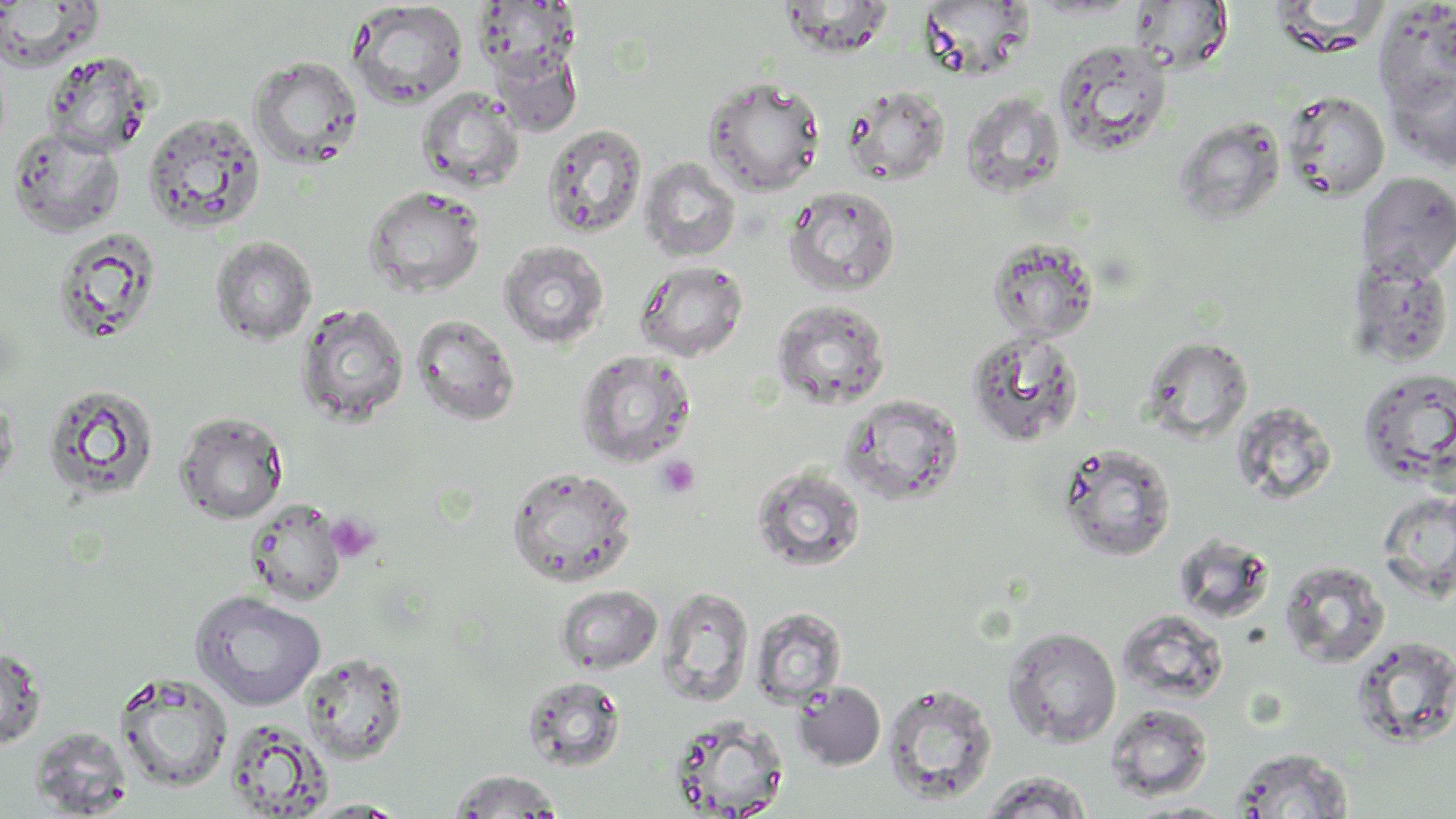

Summary:
  - Coordinate format: approximate bounding boxes as [x1, y1, x2, y2] in pixels
  - Platelet locations: [656, 455, 700, 498], [326, 513, 380, 563]
  - Uninfected red blood cell locations: [779, 0, 896, 58], [0, 1, 104, 72], [346, 1, 469, 109], [919, 1, 1035, 81], [1130, 1, 1233, 74], [475, 2, 581, 84], [1373, 2, 1456, 111], [1053, 39, 1174, 157], [493, 47, 582, 137], [43, 51, 153, 157], [248, 56, 364, 170], [1386, 67, 1456, 172], [703, 77, 825, 197], [842, 84, 951, 186], [416, 86, 524, 193], [1281, 89, 1390, 201], [959, 91, 1066, 200], [143, 112, 267, 236], [1173, 116, 1286, 226], [542, 124, 648, 239], [7, 127, 126, 238], [639, 158, 742, 262], [1356, 172, 1456, 284], [363, 185, 487, 298], [784, 185, 901, 296], [51, 228, 164, 347], [210, 236, 317, 346], [986, 237, 1099, 343], [497, 240, 610, 350], [1347, 256, 1455, 369], [634, 260, 749, 362], [771, 298, 890, 409], [295, 301, 410, 428], [411, 313, 521, 426], [965, 329, 1084, 447], [1143, 336, 1254, 441], [574, 348, 697, 468], [1356, 368, 1456, 488], [41, 383, 161, 503], [0, 390, 20, 499], [839, 394, 964, 506], [174, 411, 289, 524], [1057, 443, 1177, 562], [750, 463, 867, 573], [506, 465, 637, 587], [1376, 490, 1455, 600], [245, 498, 347, 606], [1279, 559, 1390, 668], [554, 584, 663, 674], [658, 586, 755, 707], [189, 590, 327, 710], [750, 606, 847, 708], [1118, 609, 1230, 706], [1004, 626, 1121, 747], [1349, 635, 1456, 748], [0, 646, 47, 751], [301, 651, 409, 764], [114, 672, 234, 793], [521, 674, 627, 773], [793, 682, 886, 770], [881, 682, 998, 805], [1105, 704, 1213, 801], [666, 713, 789, 818], [224, 718, 333, 817], [30, 727, 133, 817], [1230, 747, 1355, 818], [446, 769, 565, 817], [980, 771, 1095, 819], [301, 799, 411, 817], [1127, 800, 1244, 818]
  - Slide-level diagnosis: no evidence of blood parasites
  - Image size: 1456×819 pixels
  - Modality: light microscopy
  - Field of view: one of a larger specimen
  - Stain: May-Grünwald-Giemsa
  - Preparation: thin blood film
  - Magnification: 1000x